Name the blood parasite species.
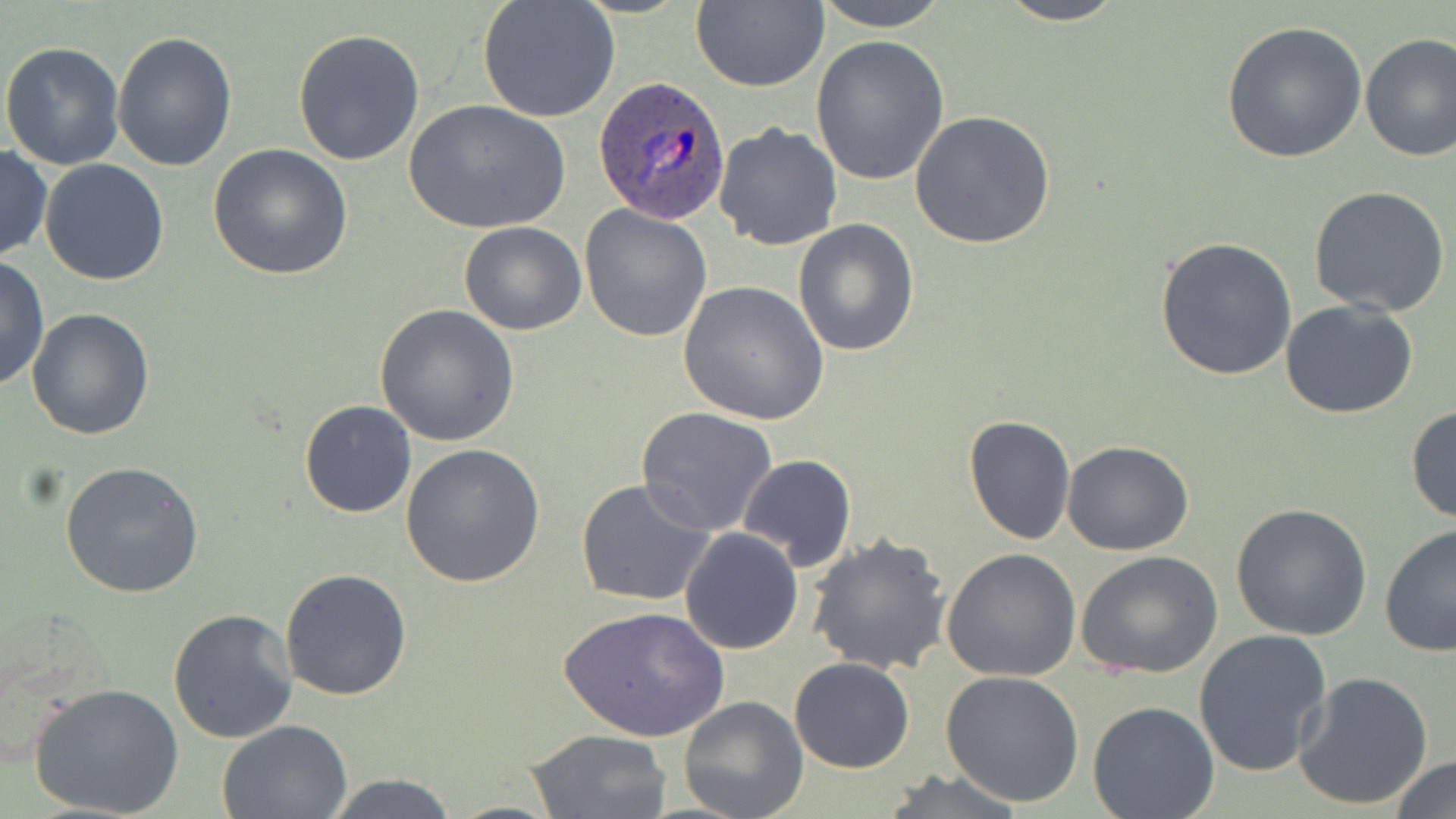
Plasmodium ovale.

magnification = 1000x
uninfected red blood cell locations = approximate bounding boxes as [x1, y1, x2, y2] in pixels: [477, 0, 621, 124], [810, 0, 951, 32], [991, 0, 1132, 25], [689, 2, 828, 92], [1221, 20, 1367, 164], [293, 27, 425, 165], [113, 31, 238, 175], [1359, 33, 1455, 162], [808, 35, 951, 185], [0, 42, 126, 169], [404, 99, 570, 235], [912, 111, 1056, 250], [712, 122, 842, 250], [0, 144, 51, 263], [208, 145, 353, 282], [39, 158, 169, 286], [1309, 186, 1450, 318], [579, 206, 713, 341], [793, 219, 921, 357], [459, 221, 586, 335], [1154, 237, 1297, 381], [0, 256, 49, 395], [677, 281, 828, 425], [1280, 299, 1421, 420], [374, 305, 520, 448], [28, 308, 154, 440], [298, 399, 417, 518], [1405, 405, 1455, 527], [637, 407, 780, 538], [962, 415, 1075, 546], [1061, 440, 1195, 555], [399, 443, 545, 588], [737, 454, 856, 574], [59, 461, 204, 598], [575, 478, 716, 608], [1230, 502, 1372, 641], [1379, 523, 1456, 658], [680, 528, 803, 655], [807, 533, 953, 675], [942, 549, 1082, 682], [1077, 551, 1223, 681], [281, 567, 413, 701], [559, 606, 728, 742], [167, 608, 299, 744], [1192, 630, 1335, 779], [789, 657, 914, 773], [939, 671, 1085, 809], [1294, 671, 1434, 811], [29, 682, 186, 819], [679, 695, 809, 819], [1086, 701, 1219, 819], [217, 719, 351, 817], [525, 728, 671, 817], [1387, 755, 1456, 819], [878, 768, 1029, 819], [320, 774, 459, 818]
stain = May-Grünwald-Giemsa
Plasmodium ovale-infected red blood cell locations = approximate bounding boxes as [x1, y1, x2, y2] in pixels: [593, 76, 731, 224]
image size = 1456×819 pixels
preparation = thin blood film
modality = light microscopy
field of view = one of a larger specimen